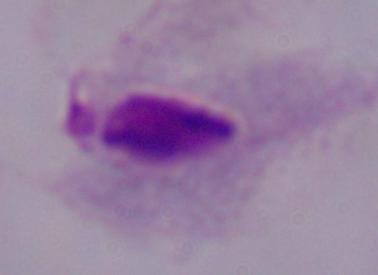

modality = micrograph
identification = trichomonad
magnification = 1000x